Name the parasite shown.
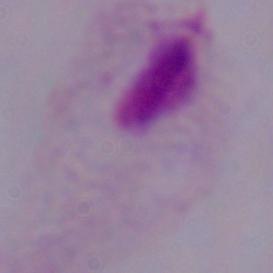
This is a trichomonad.

Summary:
  - Magnification: 1000x
  - Modality: micrograph